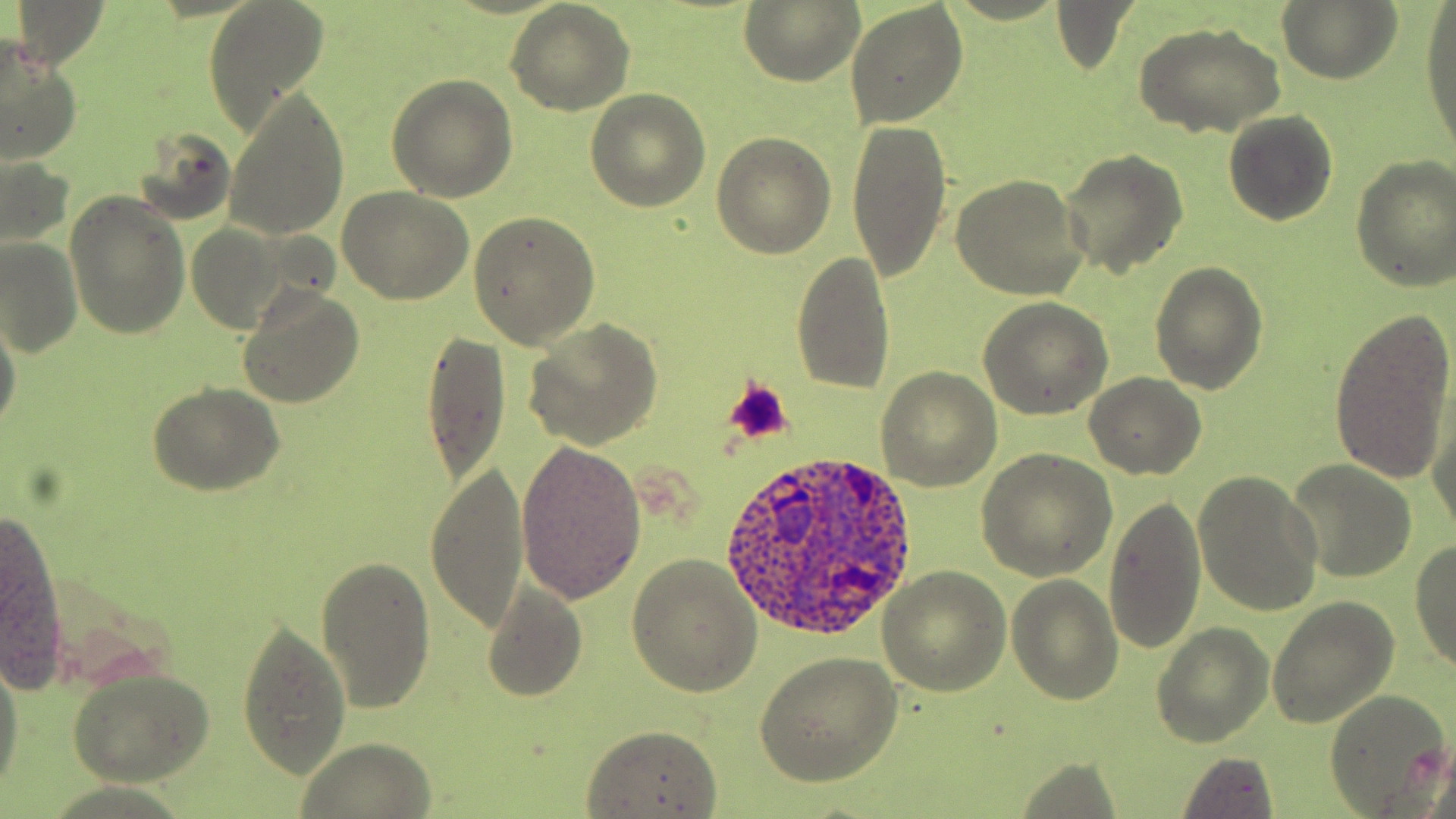
slide-level diagnosis = Plasmodium ovale
magnification = 1000x
platelet locations = approximate bounding boxes as (x1,y1)-(x2,y2) corner pairs in pixels: (722,378)-(794,445)
stain = May-Grünwald-Giemsa
uninfected red blood cell locations = approximate bounding boxes as (x1,y1)-(x2,y2) corner pairs in pixels: (7,0)-(111,72), (1050,0)-(1140,76), (1277,0)-(1402,85), (200,1)-(332,135), (739,1)-(865,87), (845,2)-(969,128), (505,3)-(636,114), (1420,6)-(1456,159), (1133,21)-(1286,137), (0,34)-(82,166), (386,74)-(518,201), (221,90)-(348,239), (585,90)-(711,211), (1223,110)-(1338,226), (846,117)-(954,280), (128,126)-(236,227), (712,133)-(836,258), (1058,151)-(1188,278), (0,154)-(76,252), (1349,156)-(1456,292), (950,174)-(1088,301), (337,185)-(475,304), (64,191)-(190,340), (469,209)-(601,347), (185,224)-(287,333), (0,233)-(83,358), (792,250)-(896,394), (1149,261)-(1267,396), (237,284)-(363,411), (977,299)-(1113,420), (0,307)-(23,441), (1331,309)-(1456,491), (524,319)-(663,450), (423,331)-(509,485), (875,368)-(1003,491), (1084,373)-(1206,480), (148,384)-(284,496), (1425,387)-(1456,545), (515,438)-(647,605), (977,448)-(1117,581), (1285,459)-(1419,584), (427,460)-(530,635), (1193,470)-(1324,617), (1103,496)-(1207,655), (2,516)-(69,686), (1409,538)-(1456,672), (626,553)-(763,697), (315,556)-(434,713), (879,568)-(1012,695), (1006,575)-(1123,704), (482,581)-(587,703), (1266,596)-(1398,729), (235,623)-(351,777), (1151,625)-(1273,748), (753,653)-(901,788), (0,655)-(23,796), (66,666)-(215,787), (1323,690)-(1453,816), (579,723)-(723,818), (296,737)-(440,818), (1173,755)-(1279,818)
image size = 1456×819 pixels
modality = optical microscopy
Plasmodium ovale-infected red blood cell locations = approximate bounding boxes as (x1,y1)-(x2,y2) corner pairs in pixels: (723,448)-(917,643)
preparation = thin blood smear
field of view = single